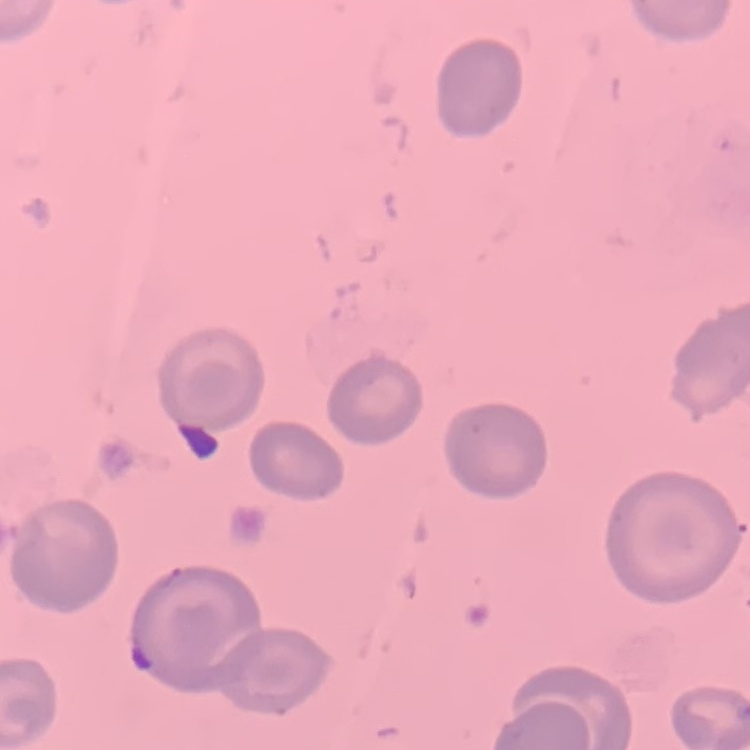
{
  "erythrocyte_morphology": "no rouleaux formation",
  "preparation": "thin blood film",
  "image_type": "square crop of a larger photomicrograph",
  "stain": "Field's or Giemsa"
}